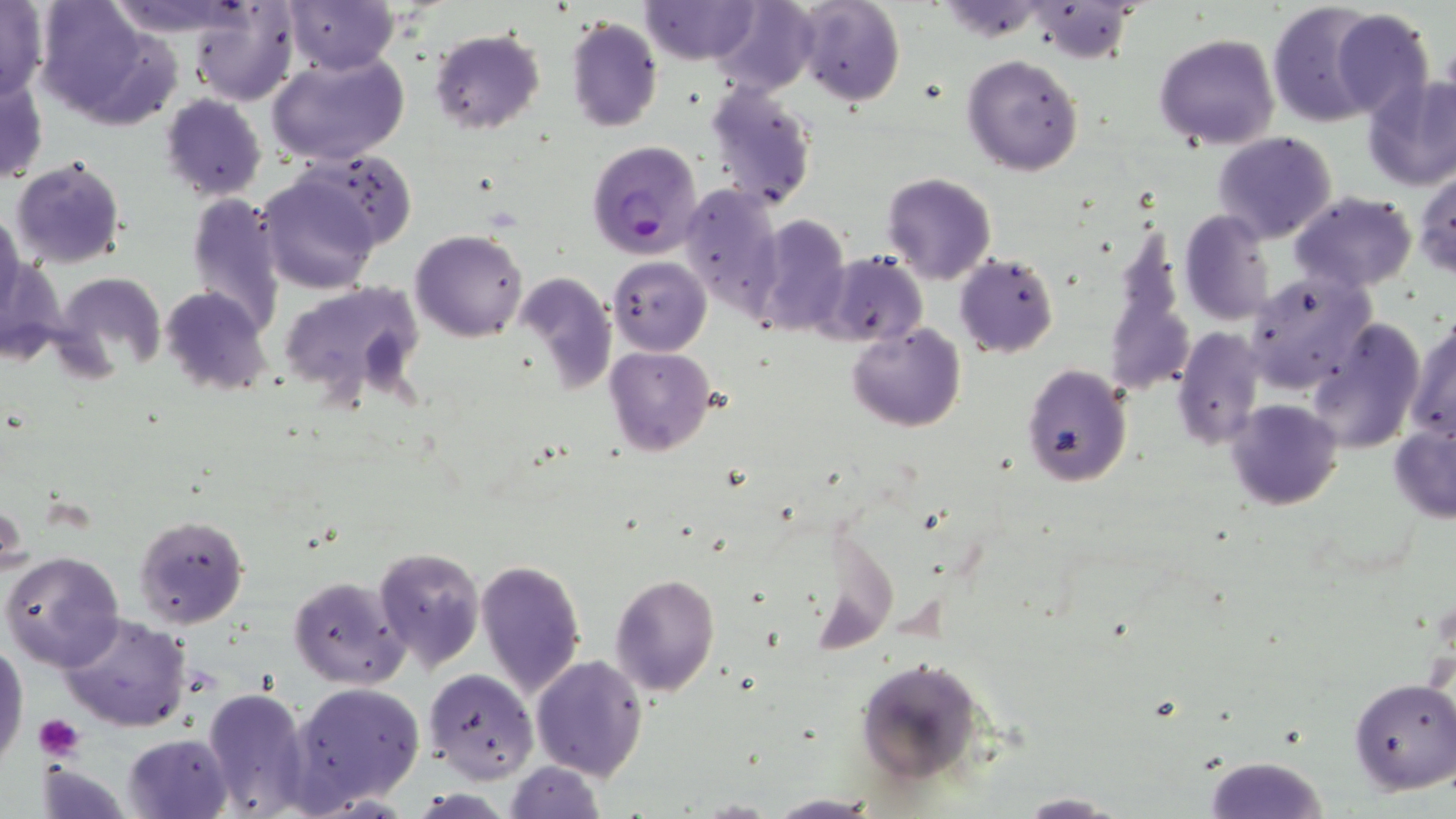
Summary:
  - Coordinate format: approximate bounding boxes as (x1,y1)-(x2,y2) corner pairs in pixels
  - Plasmodium falciparum-infected red blood cell locations: (586,139)-(703,259)
  - Platelet locations: (34,714)-(84,761)
  - Uninfected red blood cell locations: (103,0)-(253,35), (283,0)-(398,74), (710,0)-(820,96), (793,0)-(905,107), (0,1)-(49,104), (188,1)-(300,106), (640,1)-(760,65), (1267,1)-(1385,127), (35,2)-(181,127), (1030,3)-(1135,61), (1327,10)-(1435,122), (563,16)-(663,132), (429,29)-(545,133), (1154,32)-(1279,150), (267,52)-(409,168), (961,53)-(1085,175), (1361,73)-(1456,190), (0,75)-(49,186), (704,79)-(817,211), (160,94)-(267,202), (1212,131)-(1338,244), (293,148)-(416,250), (10,157)-(127,270), (1413,167)-(1455,280), (257,172)-(380,295), (881,172)-(997,285), (680,183)-(784,315), (185,192)-(285,340), (1289,192)-(1418,291), (1179,210)-(1275,326), (0,212)-(25,320), (750,214)-(851,339), (410,229)-(529,342), (816,250)-(930,346), (955,252)-(1059,358), (608,255)-(711,356), (55,271)-(168,377), (1244,271)-(1374,393), (515,275)-(617,396), (279,280)-(426,408), (159,286)-(272,397), (1404,314)-(1456,448), (1304,316)-(1424,457), (847,322)-(965,432), (1172,326)-(1264,451), (605,346)-(715,458), (1022,363)-(1130,487), (1226,399)-(1343,510), (1389,425)-(1456,523), (1,497)-(26,577), (133,513)-(248,628), (372,546)-(484,671), (2,551)-(126,673), (474,558)-(587,698), (611,573)-(721,695), (288,575)-(410,688), (56,612)-(190,733), (0,637)-(29,766), (531,654)-(648,780), (852,654)-(993,786), (422,668)-(538,783), (1349,679)-(1456,795), (289,681)-(424,808), (201,685)-(314,818), (123,734)-(234,819), (1201,755)-(1333,818), (504,761)-(605,818), (1012,793)-(1127,817), (768,795)-(877,817)
  - Slide-level diagnosis: Plasmodium falciparum
  - Magnification: 1000x
  - Modality: optical microscopy
  - Image size: 1456×819 pixels
  - Stain: May-Grünwald-Giemsa
  - Preparation: thin blood film
  - Field of view: single